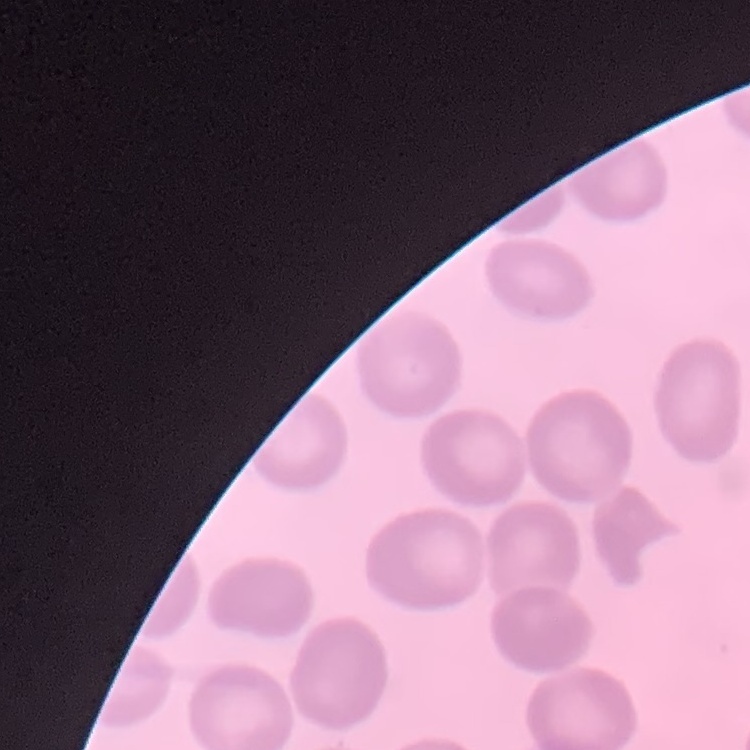
erythrocyte morphology = no rouleaux formation
stain = Field's or Giemsa
image type = square crop of a larger photomicrograph
preparation = thin blood smear